State which parasite is depicted.
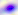

Toxoplasma gondii.

400x magnification. Photomicrograph.